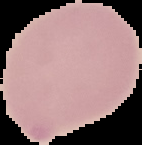

Image is 142×145 pixels. Malaria status: uninfected. Cell region segmented out of the field of view; the surrounding area is masked to black. From a thin blood film.